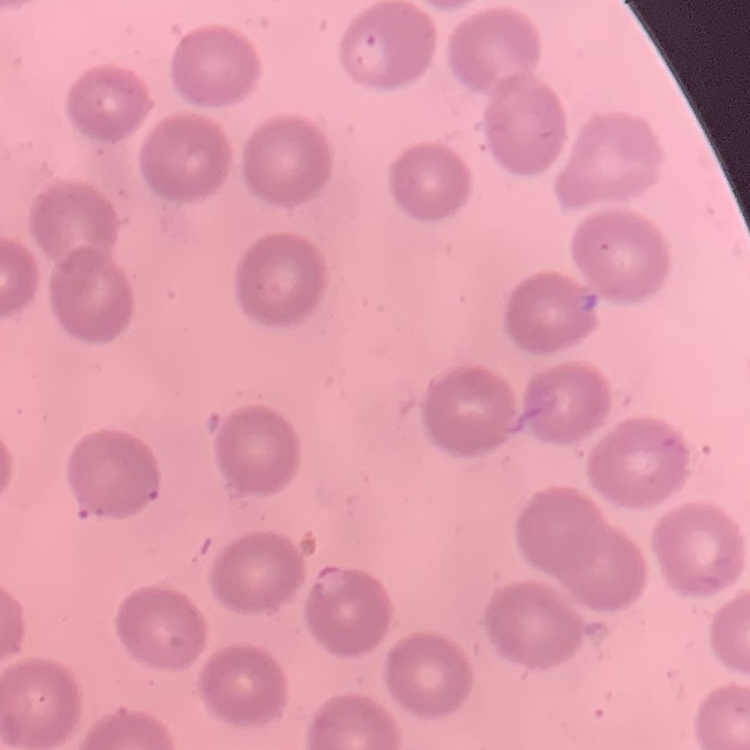
erythrocyte morphology = no rouleaux formation
stain = Field's or Giemsa
preparation = thin blood smear
image type = square crop of a larger photomicrograph